Comment on the morphology of the erythrocytes.
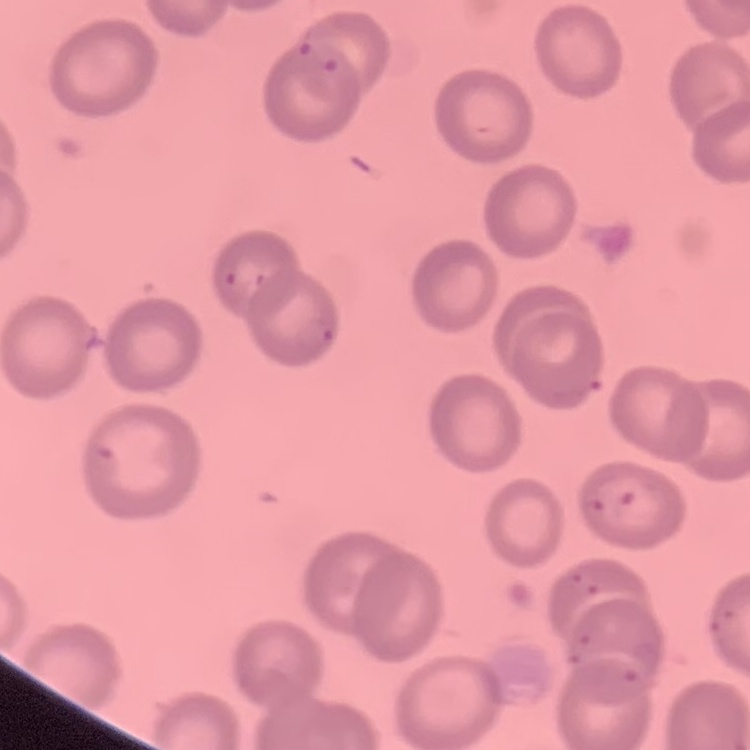
They show no rouleaux formation.

Summary:
  - Image type: square crop of a larger photomicrograph
  - Preparation: thin peripheral smear
  - Stain: Field's or Giemsa